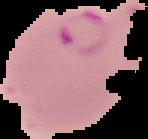
Summary:
  - Malaria status: parasitized
  - Preparation: thin blood film
  - Image type: cell region segmented out of the field of view; surrounding area masked to black
  - Image size: 148×139 pixels